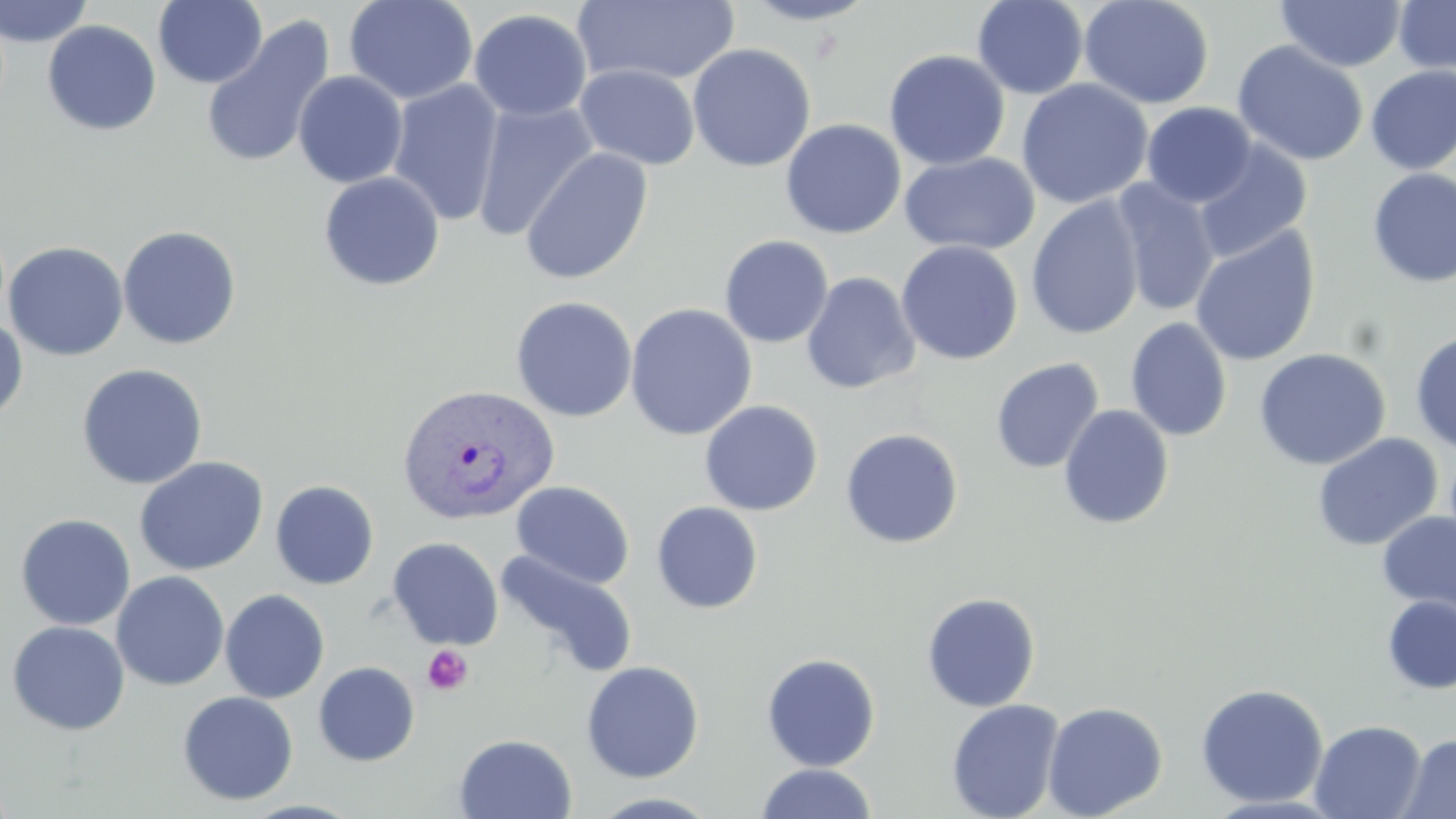

{
  "slide_level_diagnosis": "Plasmodium vivax",
  "magnification": "1000x",
  "stain": "May-Grünwald-Giemsa",
  "uninfected_red_blood_cell_locations": "approximate bounding boxes as [x1, y1, x2, y2] in pixels: [0, 0, 95, 47], [343, 0, 479, 105], [574, 0, 740, 87], [740, 0, 879, 26], [973, 0, 1088, 99], [1078, 0, 1215, 109], [1393, 0, 1456, 78], [153, 1, 268, 88], [1275, 1, 1407, 72], [468, 8, 592, 122], [200, 15, 335, 170], [42, 20, 162, 136], [1232, 40, 1369, 167], [687, 43, 816, 172], [884, 49, 1010, 171], [574, 63, 701, 170], [1365, 64, 1456, 174], [293, 70, 408, 188], [1016, 78, 1153, 209], [387, 79, 505, 227], [470, 100, 599, 242], [1141, 102, 1256, 207], [780, 118, 907, 239], [1193, 141, 1312, 263], [520, 147, 654, 285], [900, 152, 1040, 256], [1367, 168, 1456, 287], [318, 171, 445, 291], [1110, 178, 1221, 318], [1026, 196, 1145, 340], [118, 225, 242, 350], [1189, 226, 1321, 367], [719, 235, 834, 348], [896, 240, 1023, 365], [4, 241, 129, 361], [801, 272, 920, 395], [510, 296, 638, 422], [625, 303, 758, 441], [0, 314, 28, 424], [1125, 317, 1233, 442], [1409, 331, 1456, 454], [1253, 347, 1391, 471], [990, 358, 1105, 474], [76, 363, 208, 490], [699, 400, 823, 516], [1057, 404, 1174, 530], [840, 428, 964, 549], [1310, 433, 1444, 552], [133, 456, 269, 577], [270, 480, 380, 589], [511, 480, 634, 589], [651, 501, 764, 614], [1377, 511, 1456, 618], [15, 513, 136, 631], [387, 537, 503, 650], [497, 550, 638, 679], [111, 571, 229, 691], [220, 589, 330, 703], [921, 592, 1041, 712], [1382, 595, 1456, 695], [6, 621, 131, 736], [761, 652, 881, 771], [581, 660, 704, 782], [313, 661, 420, 766], [1195, 683, 1329, 808], [177, 691, 299, 806], [946, 699, 1065, 819], [1042, 701, 1167, 818], [1309, 719, 1427, 818], [1398, 732, 1456, 819], [454, 733, 577, 819], [755, 763, 877, 819]",
  "plasmodium_vivax_infected_red_blood_cell_locations": "approximate bounding boxes as [x1, y1, x2, y2] in pixels: [396, 383, 559, 527]",
  "image_size": "1456×819 pixels",
  "modality": "optical microscopy",
  "field_of_view": "single",
  "preparation": "thin blood film",
  "platelet_locations": "approximate bounding boxes as [x1, y1, x2, y2] in pixels: [422, 644, 473, 695]"
}